Report the malaria status of this cell.
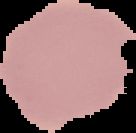

It is uninfected.

preparation = thin blood film
image type = segmented cell region on a black background
image size = 136×133 pixels